Give the extent of all uninfected red blood cells.
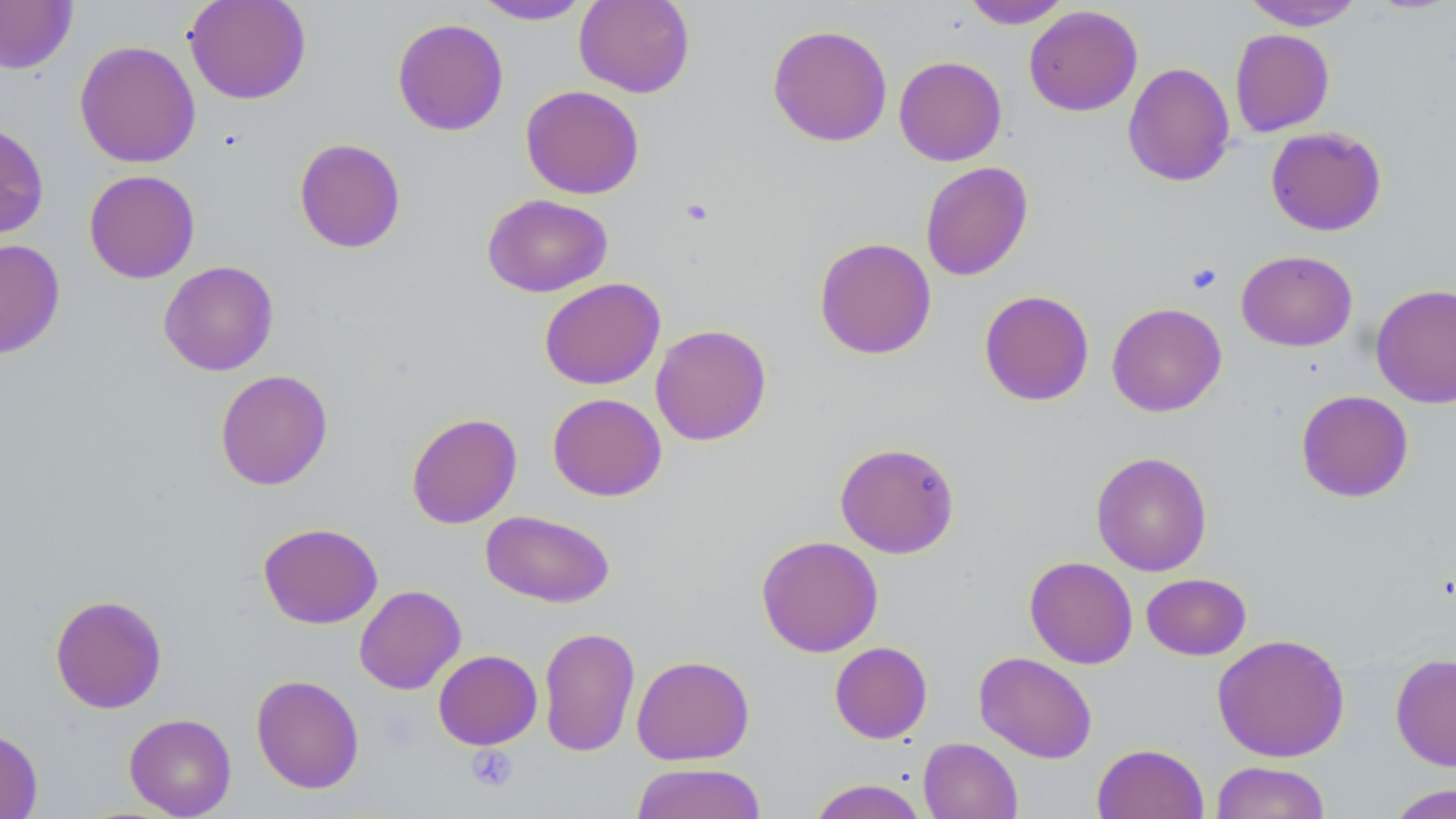
Approximate bounding boxes as (x1,y1)-(x2,y2) corner pairs in pixels.
Uninfected red blood cells: (0,0)-(78,74), (184,0)-(311,105), (574,0)-(695,97), (962,0)-(1073,29), (1241,0)-(1365,31), (470,1)-(592,25), (1024,5)-(1143,116), (392,18)-(509,136), (767,24)-(893,147), (1229,29)-(1335,136), (74,40)-(200,168), (894,56)-(1007,166), (1122,62)-(1235,188), (520,85)-(644,199), (0,120)-(49,239), (1266,126)-(1387,236), (293,137)-(406,253), (920,161)-(1033,281), (83,169)-(200,283), (482,193)-(613,297), (814,237)-(937,360), (0,239)-(66,359), (1236,250)-(1357,352), (158,260)-(279,376), (539,277)-(665,390), (1370,283)-(1456,409), (979,290)-(1094,406), (1107,302)-(1227,417), (650,323)-(772,446), (215,369)-(333,491), (1296,390)-(1414,502), (547,393)-(667,501), (406,412)-(522,529), (834,441)-(960,558), (1091,450)-(1213,576), (480,510)-(615,608), (257,522)-(383,629), (756,535)-(883,657), (1024,556)-(1138,668), (1141,572)-(1251,660), (354,585)-(466,694), (49,593)-(167,714), (538,626)-(640,758), (1212,633)-(1350,762), (829,641)-(933,744), (433,649)-(542,750), (974,651)-(1097,763), (1390,652)-(1456,771), (632,655)-(755,765), (251,674)-(364,793), (124,713)-(236,818), (0,727)-(43,819), (918,737)-(1023,819), (1092,742)-(1209,819), (1210,761)-(1331,819), (630,763)-(767,819), (807,779)-(929,819), (1382,783)-(1456,819).

Summary:
  - Platelet locations: (679,198)-(714,227), (1186,262)-(1222,294), (466,745)-(518,792)
  - Slide-level diagnosis: negative for blood parasites
  - Stain: May-Grünwald-Giemsa
  - Field of view: single
  - Magnification: 1000x
  - Image size: 1456×819 pixels
  - Modality: optical microscopy
  - Preparation: thin blood smear